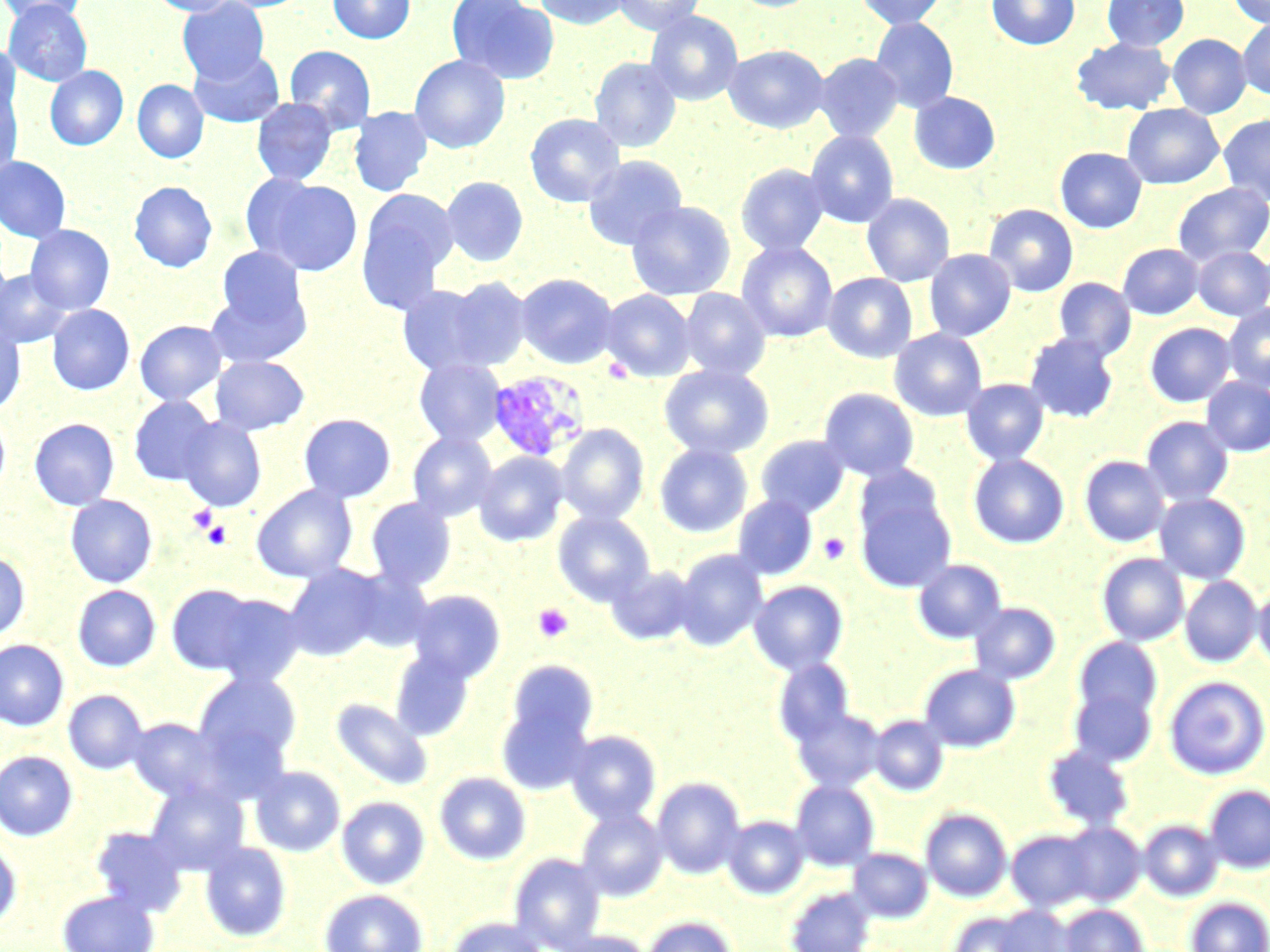

slide_level_diagnosis: Plasmodium vivax
uninfected_red_blood_cell_locations: 'approximate bounding boxes as (x1,y1)-(x2,y2) corner pairs in pixels: (0,0)-(87,27), (146,0)-(239,16), (327,0)-(415,44), (447,0)-(559,84), (533,0)-(630,29), (612,0)-(705,36), (728,0)-(822,12), (855,0)-(947,28), (987,0)-(1079,50), (1102,0)-(1189,52), (1228,0)-(1270,27), (177,1)-(269,84), (4,2)-(92,85), (645,11)-(744,106), (869,17)-(958,114), (1237,18)-(1270,99), (1167,34)-(1252,118), (1071,37)-(1176,115), (0,43)-(21,125), (284,44)-(376,133), (723,45)-(829,134), (188,48)-(285,128), (814,53)-(903,143), (409,55)-(510,154), (589,57)-(681,153), (45,65)-(128,150), (132,79)-(209,163), (0,86)-(23,185), (909,92)-(1000,174), (251,98)-(338,186), (1122,103)-(1224,189), (348,106)-(433,196), (525,113)-(625,208), (1218,114)-(1270,205), (805,130)-(899,228), (1055,147)-(1147,233), (583,155)-(687,250), (0,156)-(71,243), (735,163)-(829,255), (441,176)-(528,267), (253,177)-(364,276), (129,181)-(217,272), (256,181)-(458,291), (1172,182)-(1270,266), (357,189)-(459,310), (862,193)-(955,287), (626,200)-(735,301), (984,204)-(1079,296), (25,224)-(115,315), (736,242)-(838,343), (1118,243)-(1203,319), (216,247)-(309,332), (1193,247)-(1270,321), (924,249)-(1016,341), (0,269)-(71,348), (515,272)-(618,369), (823,272)-(918,363), (441,276)-(532,371), (1053,277)-(1136,360), (396,283)-(500,375), (679,288)-(771,381), (205,289)-(309,369), (600,290)-(695,383), (1223,303)-(1270,391), (46,304)-(135,395), (135,320)-(227,405), (0,321)-(26,415), (1144,322)-(1236,407), (889,328)-(988,422), (1024,332)-(1119,423), (209,354)-(309,435), (413,358)-(506,447), (659,364)-(774,460), (1201,376)-(1270,456), (961,378)-(1049,466), (818,388)-(919,482), (128,395)-(218,486), (0,410)-(11,502), (298,413)-(396,503), (1140,416)-(1234,506), (178,417)-(267,512), (29,418)-(120,510), (555,424)-(648,526), (407,431)-(498,522), (755,435)-(850,518), (654,443)-(753,538), (473,451)-(568,547), (968,454)-(1069,548), (1079,455)-(1170,547), (856,463)-(947,545), (854,481)-(956,594), (251,484)-(358,583), (1154,492)-(1251,583), (65,494)-(157,588), (732,494)-(818,580), (365,498)-(457,592), (553,511)-(656,607), (673,548)-(769,651), (0,551)-(30,643), (1096,553)-(1190,646), (912,559)-(1007,644), (283,564)-(386,661), (606,564)-(699,646), (345,568)-(434,652), (1179,576)-(1263,667), (748,580)-(848,675), (1254,581)-(1270,676), (166,583)-(265,675), (72,585)-(161,672), (406,589)-(505,683), (207,593)-(307,687), (969,602)-(1061,684), (1072,637)-(1163,724), (0,639)-(69,731), (389,649)-(476,742), (772,658)-(855,746), (506,659)-(598,748), (918,664)-(1020,752), (194,670)-(302,771), (1163,675)-(1269,780), (1067,684)-(1158,767), (63,690)-(148,774), (331,697)-(434,791), (496,702)-(594,795), (792,707)-(886,792), (870,714)-(949,796), (127,717)-(228,803), (565,730)-(661,825), (1042,744)-(1134,831), (0,750)-(78,841), (250,765)-(346,857), (434,771)-(531,865), (652,776)-(747,879), (789,780)-(879,871), (145,781)-(249,876), (1203,785)-(1270,873), (337,795)-(430,890), (574,806)-(668,901), (920,808)-(1012,901), (722,815)-(810,899), (1138,819)-(1223,901), (1057,822)-(1146,906), (91,826)-(190,917), (1006,829)-(1099,912), (0,838)-(22,930), (199,842)-(292,942), (848,848)-(933,922), (509,852)-(606,951), (783,886)-(877,952), (319,889)-(427,952), (57,890)-(159,952), (1185,896)-(1270,952), (1059,904)-(1149,952), (984,905)-(1077,952), (946,910)-(1040,952), (640,915)-(738,952), (448,916)-(548,952), (550,930)-(654,952)'
plasmodium_vivax_infected_red_blood_cell_locations: 'approximate bounding boxes as (x1,y1)-(x2,y2) corner pairs in pixels: (487,369)-(591,463)'
magnification: 1000x
stain: May-Grünwald-Giemsa
field_of_view: single
platelet_locations: 'approximate bounding boxes as (x1,y1)-(x2,y2) corner pairs in pixels: (188,505)-(218,533), (201,521)-(232,549), (818,533)-(850,565), (533,603)-(573,643)'
modality: light microscopy
image_size: 1270×952 pixels
preparation: thin blood smear